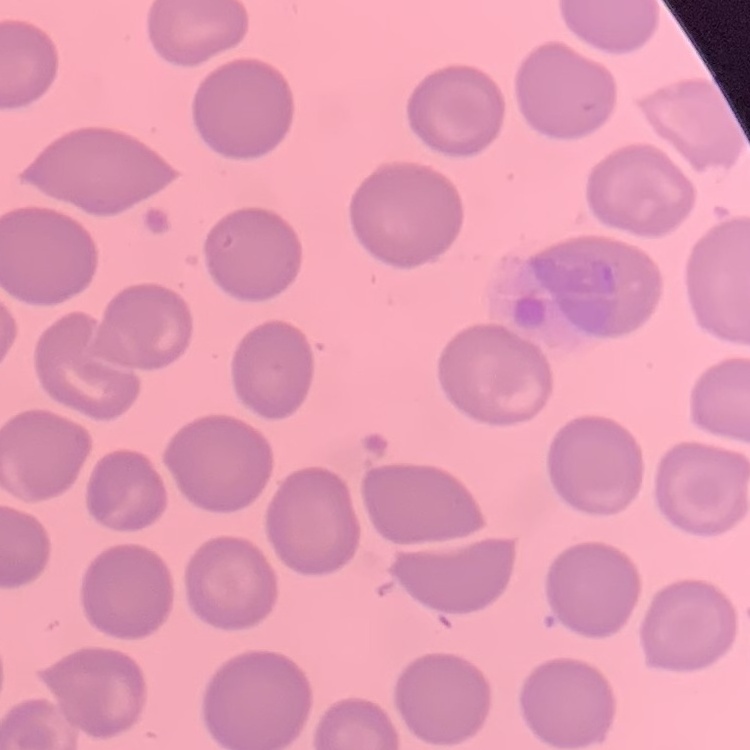
Summary:
  - Red blood cell morphology: no rouleaux formation
  - Image type: square crop of a larger photomicrograph
  - Preparation: thin blood smear
  - Stain: Field's or Giemsa